Classify this cell by malaria status.
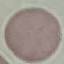

It is uninfected.

Acquired by smartphone through the microscope eyepiece. Automatically extracted cell patch, resized to 64 × 64 pixels. Thin blood smear. Giemsa stain.